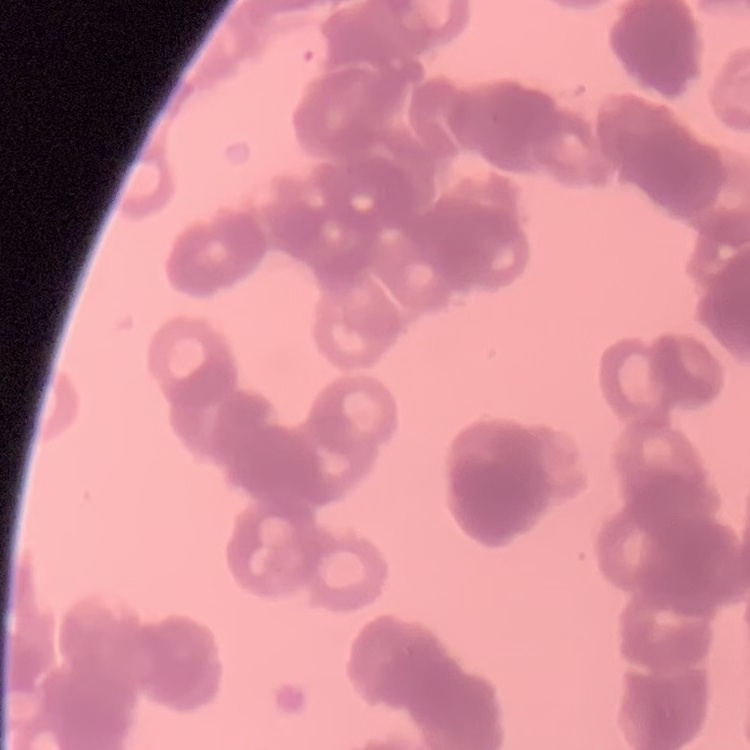

red blood cell morphology = rouleaux formation
stain = Field's or Giemsa
preparation = thin blood film
image type = one tile cut from a larger photomicrograph